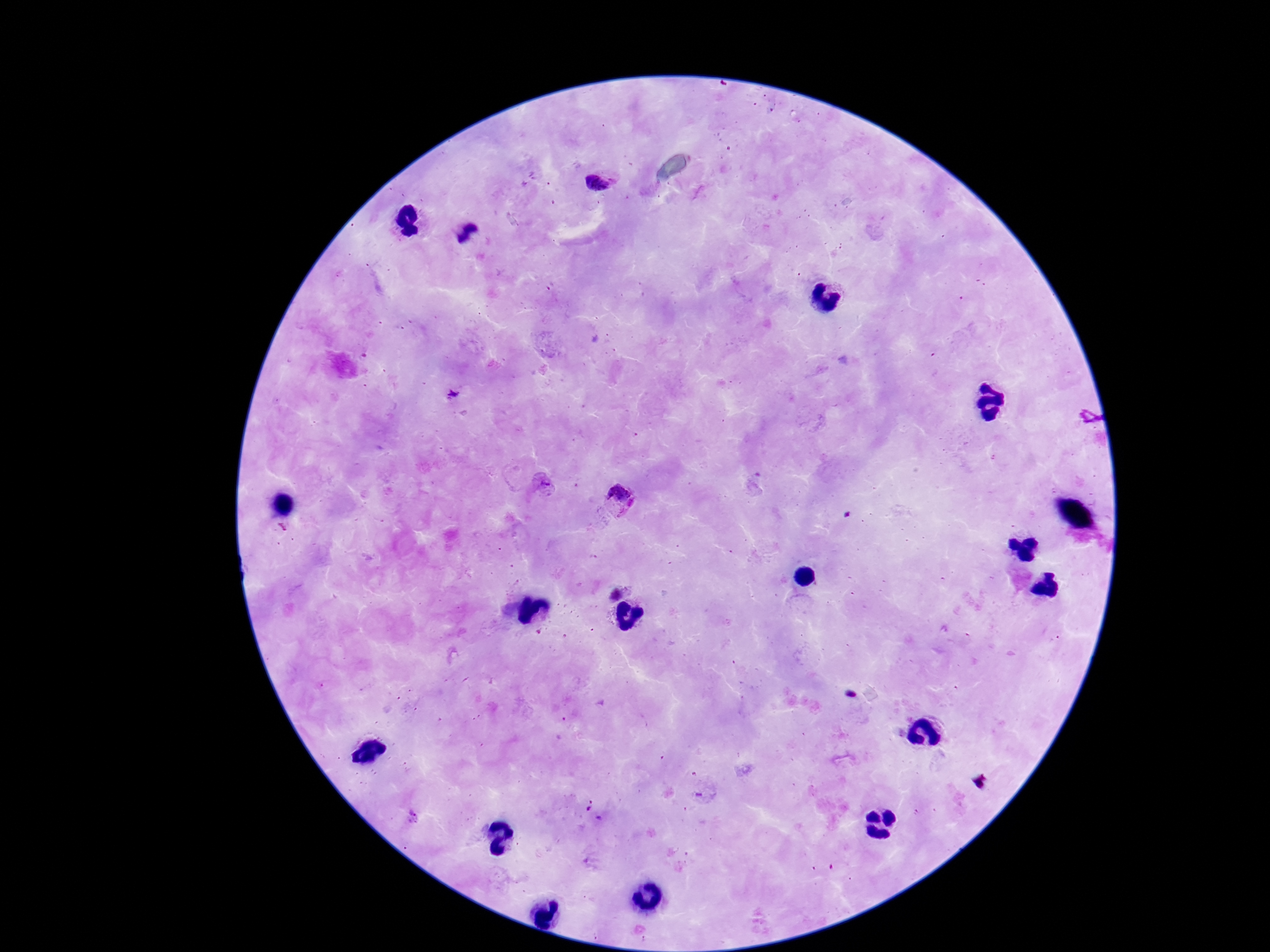
{
  "field_of_view": "one from this slide",
  "stain": "Giemsa",
  "plasmodium_parasite_locations": "approximate object centers, in pixels from the top-left corner: (x=598, y=182), (x=451, y=393), (x=544, y=485), (x=618, y=502)",
  "image_size": "1270×952 pixels",
  "magnification": "100x",
  "capture": "smartphone camera through the microscope eyepiece",
  "patient_malaria_status": "infected",
  "preparation": "thick blood film"
}